Outline each uninfected red blood cell.
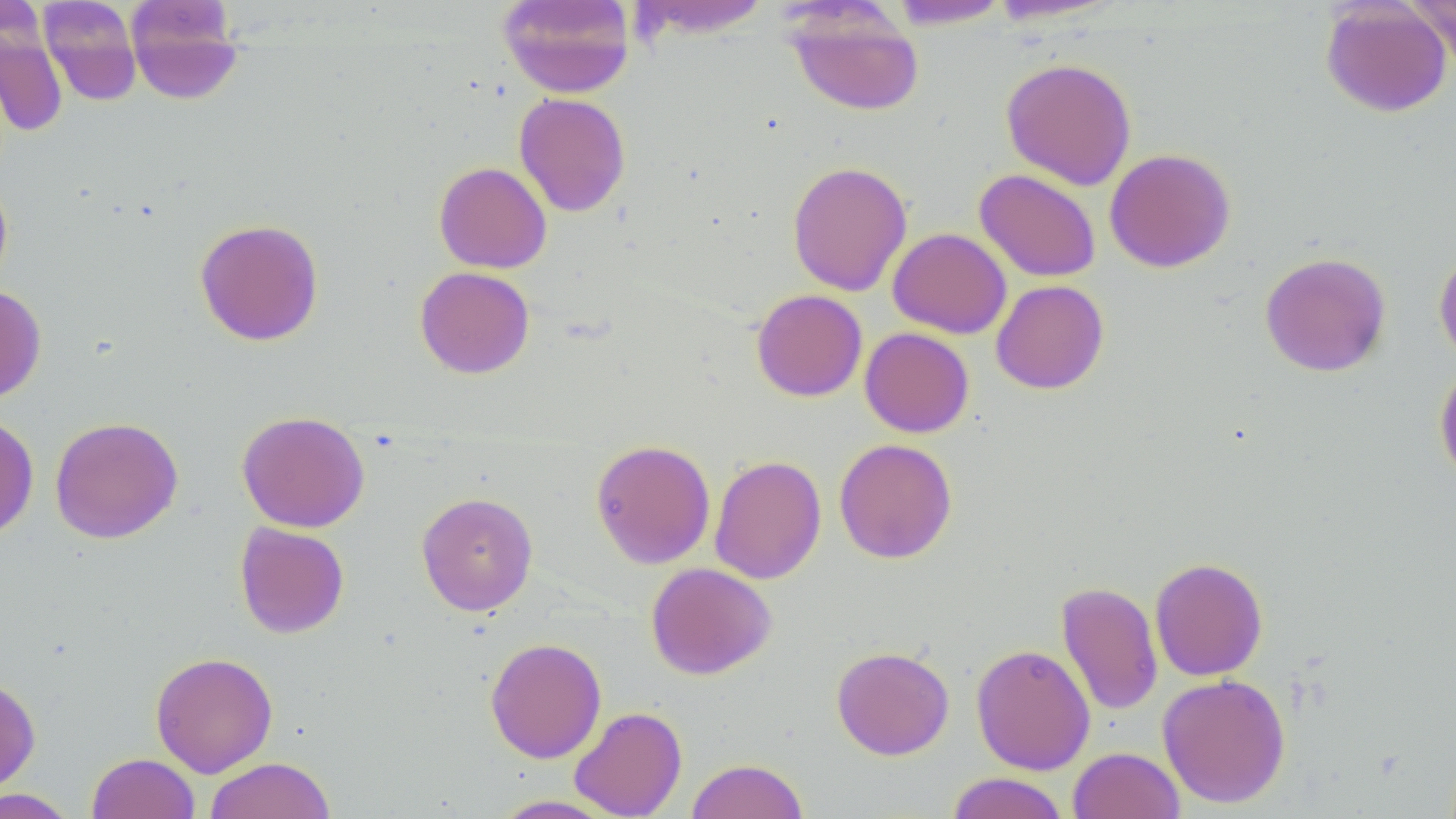

Approximate bounding boxes as named x1/y1/x2/y2 corners in pixels.
Uninfected red blood cells: (x1=38, y1=0, x2=142, y2=105), (x1=124, y1=0, x2=245, y2=105), (x1=986, y1=0, x2=1127, y2=25), (x1=1407, y1=0, x2=1456, y2=74), (x1=496, y1=1, x2=636, y2=98), (x1=631, y1=1, x2=773, y2=40), (x1=886, y1=1, x2=1012, y2=29), (x1=1320, y1=1, x2=1452, y2=118), (x1=786, y1=6, x2=924, y2=117), (x1=0, y1=23, x2=68, y2=137), (x1=1001, y1=57, x2=1137, y2=190), (x1=514, y1=92, x2=631, y2=217), (x1=1105, y1=148, x2=1236, y2=273), (x1=787, y1=160, x2=912, y2=297), (x1=434, y1=161, x2=552, y2=273), (x1=974, y1=168, x2=1101, y2=282), (x1=0, y1=175, x2=13, y2=296), (x1=194, y1=218, x2=324, y2=346), (x1=888, y1=228, x2=1012, y2=338), (x1=1433, y1=249, x2=1456, y2=365), (x1=1259, y1=252, x2=1391, y2=377), (x1=415, y1=266, x2=535, y2=379), (x1=991, y1=279, x2=1109, y2=394), (x1=0, y1=285, x2=47, y2=404), (x1=751, y1=289, x2=867, y2=402), (x1=859, y1=327, x2=974, y2=437), (x1=1433, y1=363, x2=1456, y2=485), (x1=236, y1=410, x2=370, y2=533), (x1=0, y1=413, x2=39, y2=541), (x1=49, y1=416, x2=183, y2=544), (x1=590, y1=438, x2=716, y2=569), (x1=834, y1=438, x2=957, y2=563), (x1=709, y1=454, x2=827, y2=585), (x1=416, y1=491, x2=538, y2=615), (x1=234, y1=522, x2=349, y2=638), (x1=1149, y1=557, x2=1268, y2=681), (x1=646, y1=562, x2=776, y2=680), (x1=1056, y1=581, x2=1163, y2=716), (x1=485, y1=636, x2=607, y2=764), (x1=971, y1=643, x2=1095, y2=775), (x1=831, y1=645, x2=954, y2=760), (x1=150, y1=651, x2=278, y2=777), (x1=1157, y1=673, x2=1291, y2=808), (x1=0, y1=677, x2=41, y2=794), (x1=569, y1=705, x2=687, y2=819), (x1=1067, y1=746, x2=1184, y2=819), (x1=87, y1=752, x2=200, y2=819), (x1=204, y1=757, x2=336, y2=819), (x1=686, y1=758, x2=810, y2=819), (x1=945, y1=772, x2=1070, y2=819), (x1=0, y1=788, x2=79, y2=818), (x1=489, y1=794, x2=620, y2=818).

{
  "slide_level_diagnosis": "no evidence of blood parasites",
  "field_of_view": "one of a larger specimen",
  "modality": "optical microscopy",
  "stain": "May-Grünwald-Giemsa",
  "magnification": "1000x",
  "preparation": "thin blood film",
  "image_size": "1456×819 pixels"
}